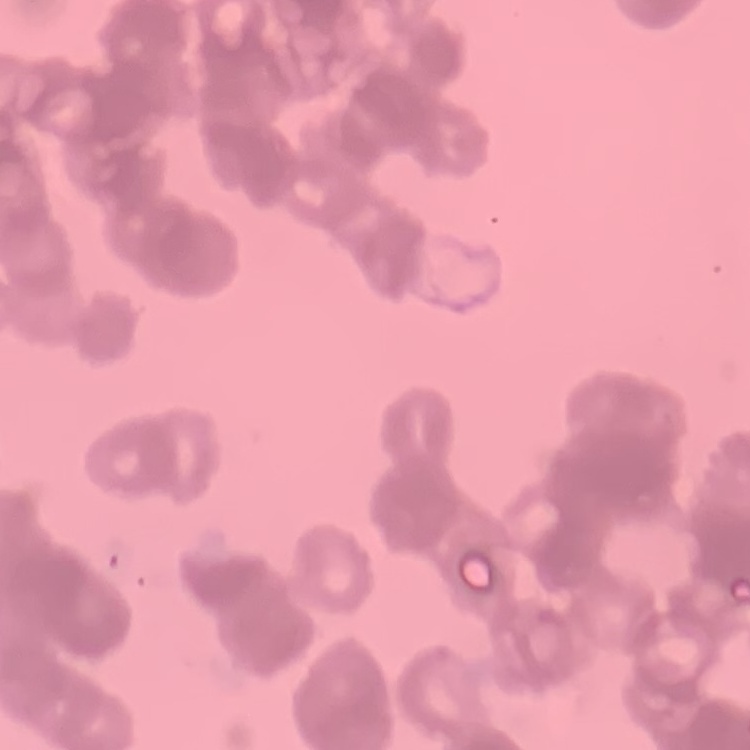
Summary:
  - Red blood cell morphology: rouleaux formation
  - Stain: Field's or Giemsa
  - Image type: one tile cut from a larger photomicrograph
  - Preparation: thin peripheral smear